Assess this cell for malaria.
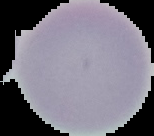

It is uninfected.

Summary:
  - Image size: 154×136 pixels
  - Image type: segmented cell region with the area outside set to black
  - Preparation: thin blood film